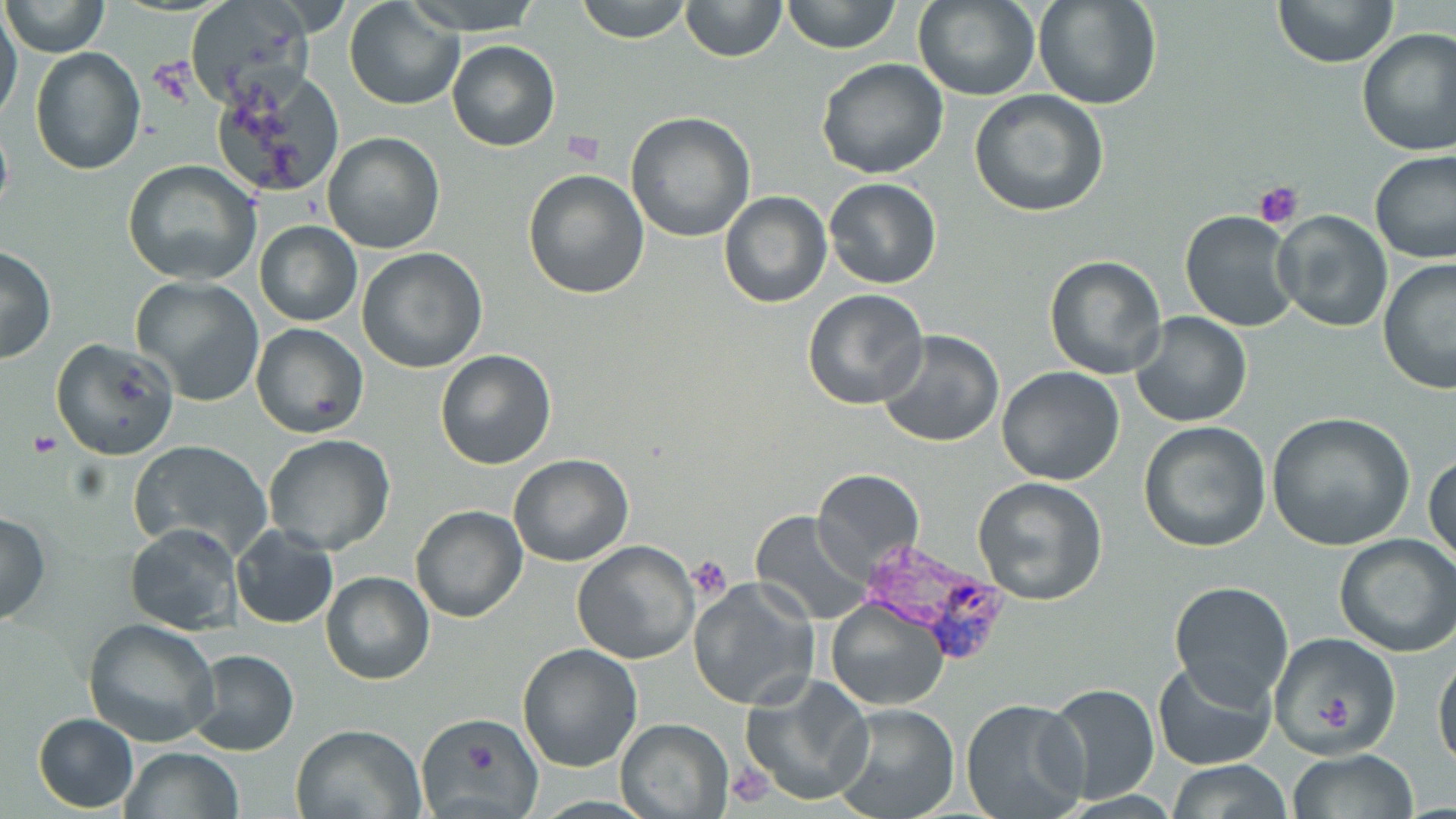 Approximate bounding boxes as (x1,y1)-(x2,y2) corner pairs in pixels. Plasmodium vivax-infected red blood cell locations: (853,537)-(1012,663). Platelet locations: (561,131)-(604,165), (1251,177)-(1306,228), (27,429)-(60,457), (687,556)-(734,601), (1318,695)-(1354,734), (729,764)-(775,807). Uninfected red blood cell locations: (3,0)-(109,58), (344,0)-(465,111), (402,0)-(545,33), (574,0)-(694,44), (678,0)-(788,63), (781,0)-(902,55), (912,0)-(1040,101), (1034,0)-(1163,110), (1272,0)-(1399,69), (185,2)-(311,103), (0,9)-(22,124), (1356,28)-(1456,157), (447,40)-(561,151), (30,46)-(146,176), (816,59)-(949,180), (210,69)-(349,199), (969,89)-(1109,217), (624,112)-(756,244), (323,132)-(445,254), (1369,147)-(1456,264), (121,159)-(263,284), (522,168)-(651,299), (824,177)-(942,290), (719,193)-(831,308), (1180,210)-(1302,332), (1273,210)-(1395,333), (255,221)-(361,327), (358,246)-(488,374), (0,247)-(57,364), (1043,253)-(1167,378), (1378,258)-(1456,394), (131,275)-(264,406), (803,289)-(929,410), (1131,312)-(1253,427), (250,323)-(370,438), (877,328)-(1004,447), (49,337)-(180,461), (435,349)-(557,470), (997,366)-(1126,485), (1266,411)-(1415,550), (1138,420)-(1272,553), (263,435)-(395,554), (129,440)-(272,562), (1425,452)-(1456,571), (508,453)-(634,567), (811,469)-(926,580), (973,476)-(1109,605), (410,504)-(527,622), (0,510)-(50,625), (751,510)-(870,626), (125,522)-(241,635), (230,524)-(339,629), (1334,533)-(1456,658), (572,540)-(700,665), (319,572)-(434,686), (688,576)-(819,711), (1168,581)-(1294,703), (824,596)-(948,711), (83,618)-(221,746), (1271,635)-(1405,760), (515,643)-(642,772), (1432,645)-(1456,769), (189,649)-(299,755), (1151,659)-(1278,771), (739,673)-(875,807), (1044,682)-(1162,806), (959,699)-(1090,819), (831,704)-(960,819), (33,712)-(139,813), (416,712)-(543,819), (617,718)-(733,818), (291,722)-(424,817), (118,746)-(245,819), (1285,751)-(1420,819), (1162,760)-(1297,817). Slide-level diagnosis: Plasmodium vivax. Thin blood film. Single field of view. Image is 1456×819 pixels. May-Grünwald-Giemsa-stained preparation. Light microscopy. 1000x magnification.